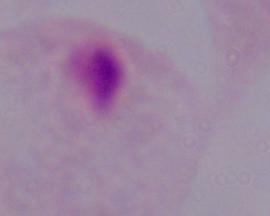 A trichomonad is shown. Micrograph. Captured at 1000x magnification.